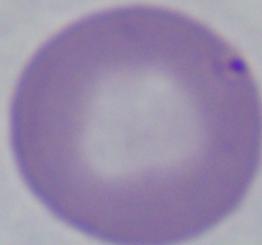

Summary:
  - Modality: photomicrograph
  - Magnification: 1000x
  - Identification: Babesia